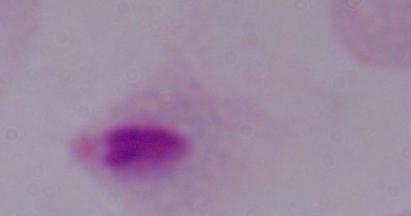

Summary:
  - Modality: photomicrograph
  - Identification: trichomonad
  - Magnification: 1000x